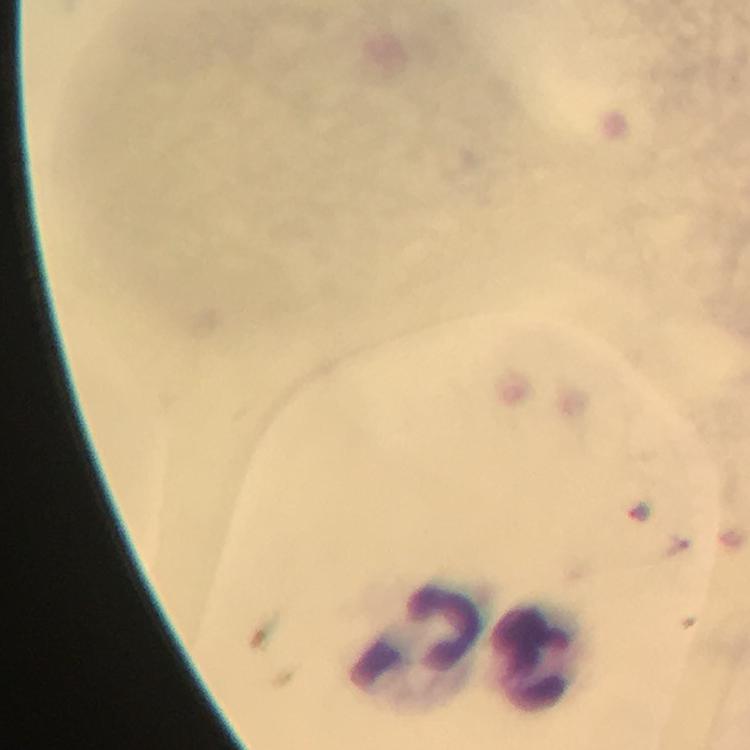

Approximate centers as [x, y] in pixels.
Summary:
  - Leukocyte locations: [419, 645], [538, 657]
  - Image size: 750×750 pixels
  - Capture: smartphone mounted on the microscope
  - Malaria parasites: none detected
  - Stain: Giemsa
  - Magnification: 100x
  - Preparation: thick blood film
  - Cropped from: a single field of view
  - Immersion oil: applied
  - Context: from a diagnostic examination for malaria